Name the malaria species.
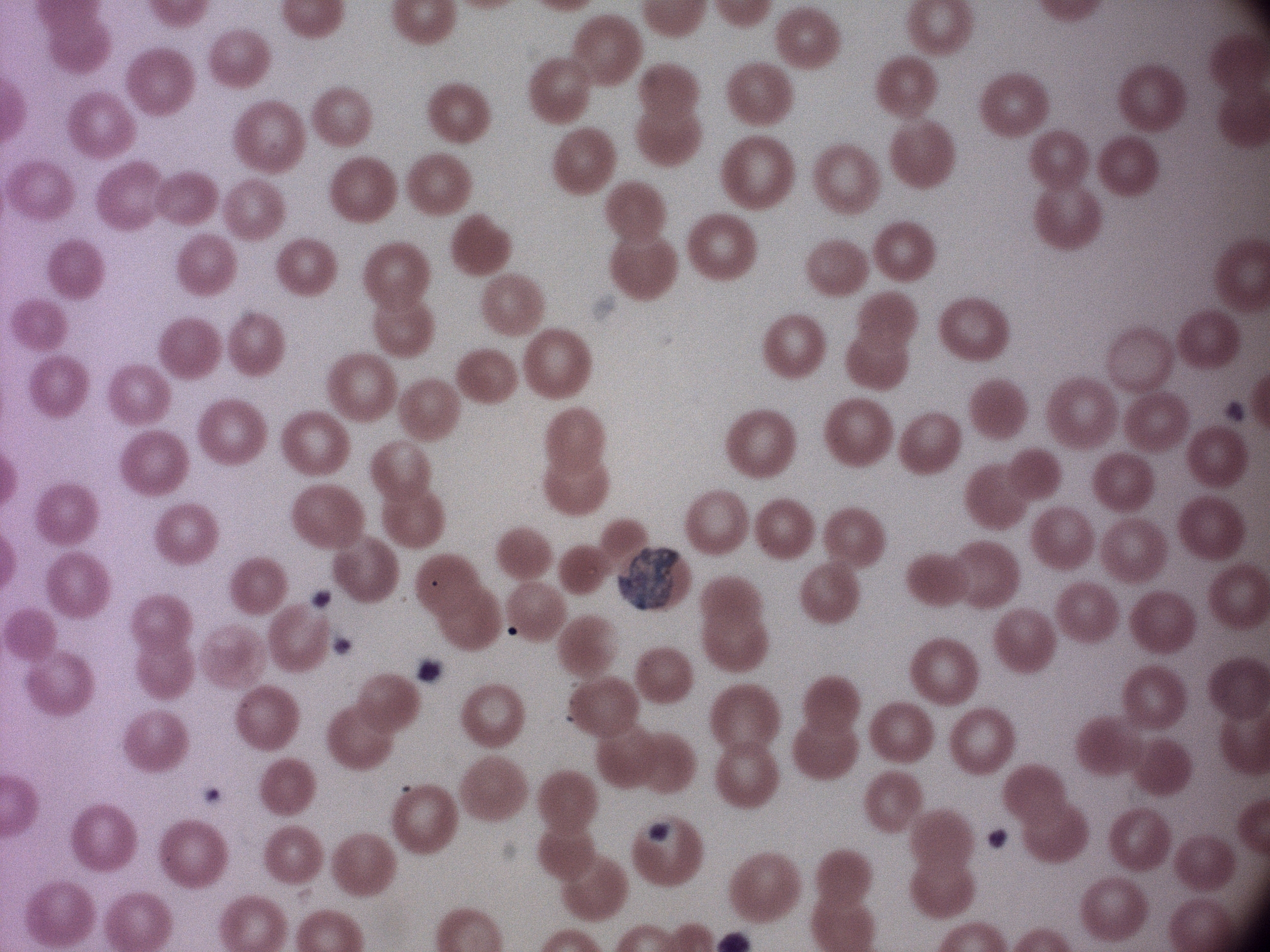

Plasmodium malariae.

Approximate bounding boxes as named x1/y1/x2/y2 corners in pixels, from the source annotation, which is not necessarily exhaustive.
Summary:
  - Gametocyte locations: (x1=617, y1=547, x2=682, y2=611), (x1=646, y1=822, x2=672, y2=842)
  - Magnification: 100x
  - Preparation: thin blood smear
  - Field of view: single
  - Image size: 1270×952 pixels
  - Microscope: Leica DM2000 with built-in camera
  - Stain: Giemsa